Give the position of every malaria parasite.
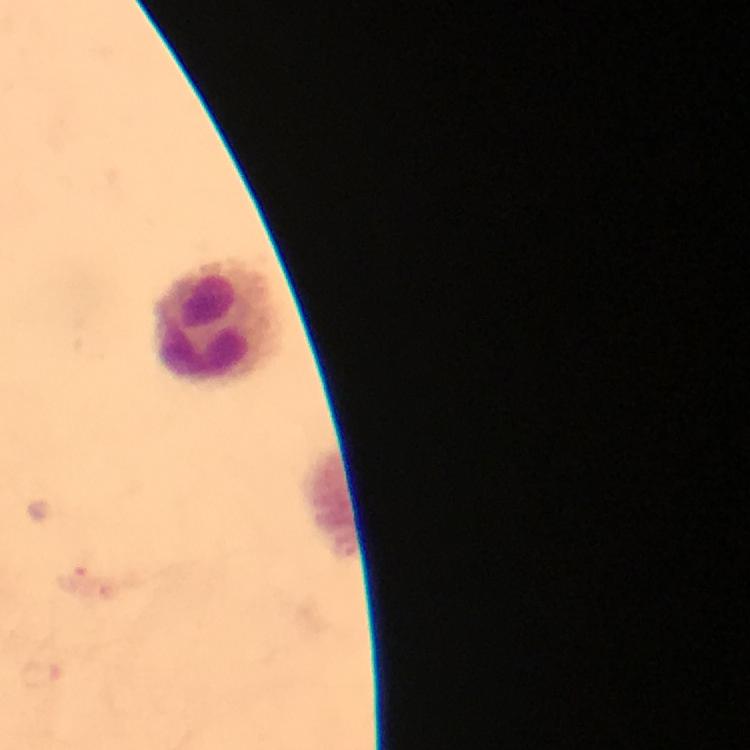

No malaria parasites detected.

Approximate centers as [x, y] in pixels.
Summary:
  - Leukocyte locations: [221, 321]
  - Magnification: 100x
  - Context: from a malaria diagnostic workup
  - Cropped from: a single field of view
  - Immersion oil: applied
  - Preparation: thick smear
  - Stain: Giemsa
  - Capture: smartphone photograph through a microscope
  - Image size: 750×750 pixels